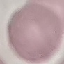

Summary:
  - Result: negative for malaria parasites
  - Preparation: thin smear
  - Image type: cell patch, automatically extracted from a larger field of view and resized to 64 × 64 pixels
  - Stain: Giemsa
  - Capture: smartphone camera at the microscope eyepiece